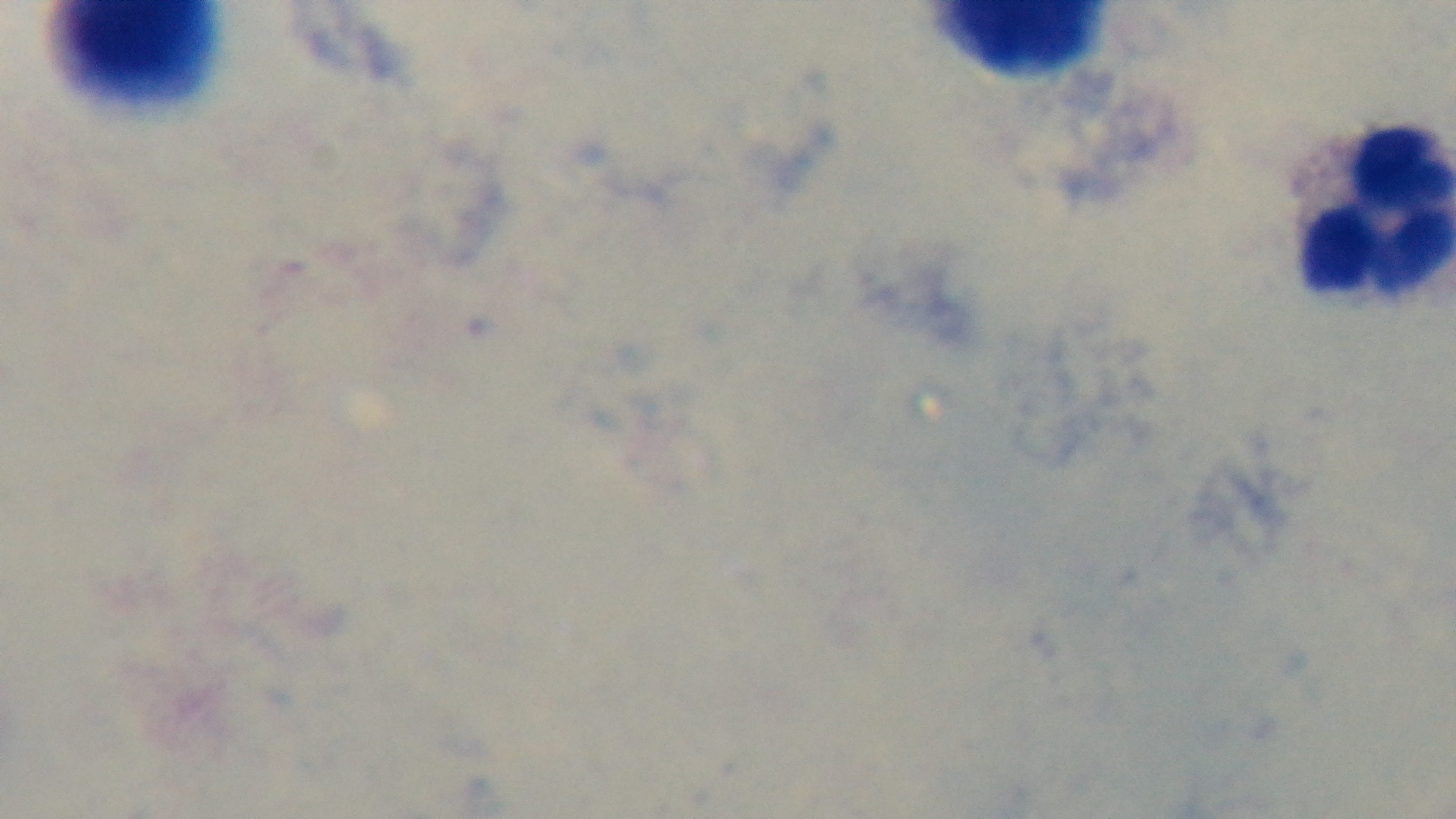
field of view = single
capture = mounted 4K digital camera
malaria status = negative
stain = Giemsa
preparation = thick smear
modality = light microscopy
objective = 100x oil immersion